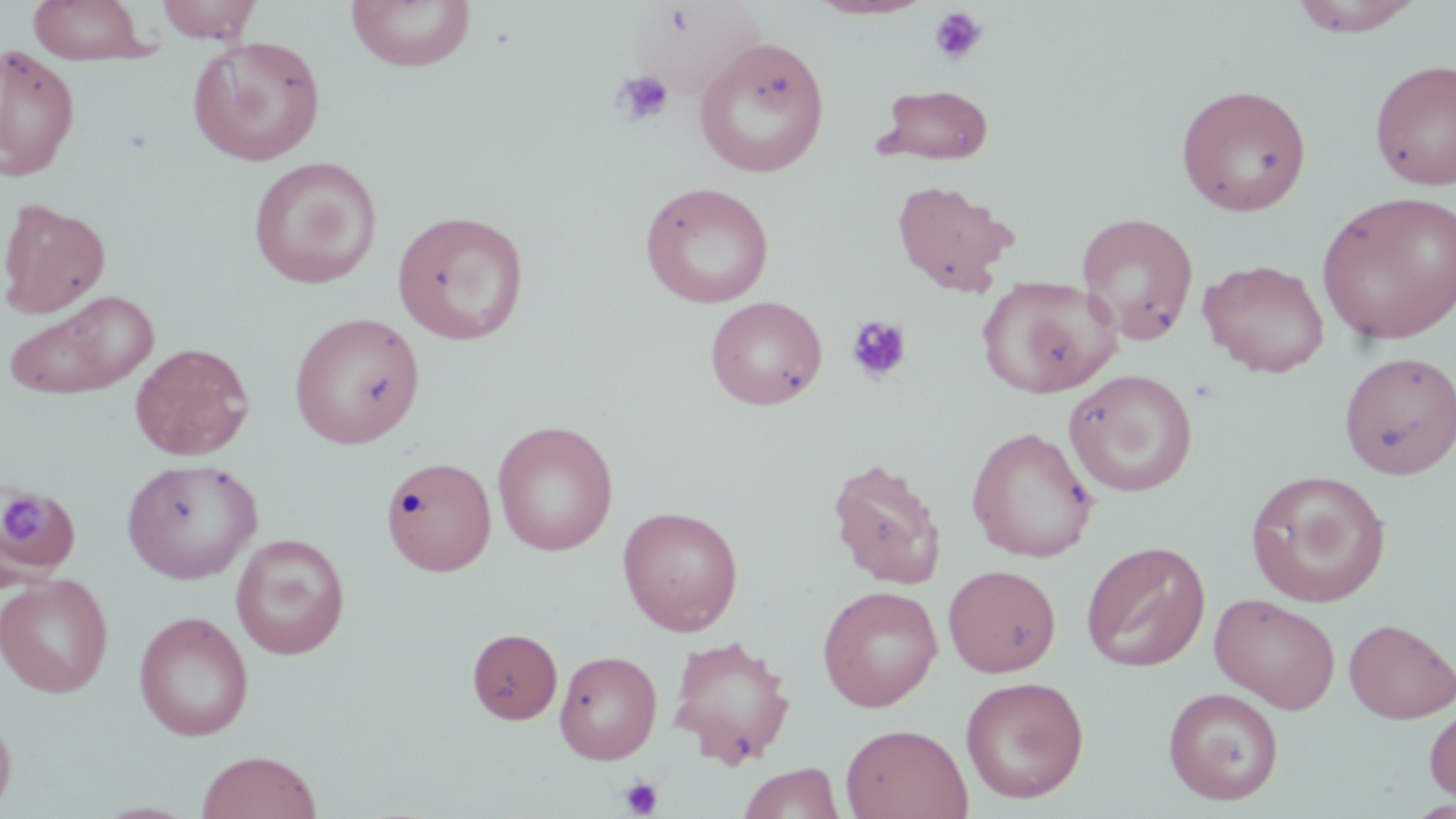

Summary:
  - Coordinate format: approximate bounding boxes as (x1, y1, x2, y2) in pixels
  - Uninfected red blood cell locations: (26, 0, 156, 65), (154, 0, 263, 43), (345, 0, 476, 73), (805, 0, 935, 20), (1289, 0, 1426, 37), (633, 4, 766, 99), (187, 35, 326, 166), (693, 37, 831, 178), (0, 44, 80, 181), (1370, 58, 1456, 190), (874, 84, 995, 165), (1176, 84, 1312, 217), (248, 156, 382, 289), (890, 179, 1019, 296), (639, 181, 776, 308), (1316, 189, 1456, 346), (0, 197, 110, 319), (391, 209, 530, 345), (1076, 211, 1200, 345), (1199, 259, 1330, 378), (976, 274, 1121, 399), (3, 290, 159, 400), (705, 295, 828, 410), (289, 311, 425, 449), (129, 342, 255, 461), (1338, 350, 1456, 478), (1063, 368, 1199, 497), (492, 420, 619, 556), (966, 426, 1099, 563), (381, 456, 496, 576), (827, 457, 947, 588), (121, 458, 263, 584), (1245, 470, 1391, 607), (0, 482, 80, 583), (617, 506, 744, 636), (230, 533, 351, 660), (1081, 540, 1211, 672), (943, 564, 1062, 677), (0, 574, 113, 698), (817, 585, 943, 711), (1210, 593, 1341, 713), (133, 611, 254, 742), (1343, 618, 1456, 723), (466, 627, 563, 724), (666, 633, 797, 768), (554, 650, 662, 763), (960, 675, 1089, 803), (1163, 686, 1285, 805), (1424, 703, 1456, 806), (0, 708, 16, 815), (840, 723, 973, 819), (196, 749, 322, 819), (737, 762, 845, 819)
  - Platelet locations: (927, 7, 988, 66), (612, 70, 674, 128), (845, 315, 913, 384), (3, 491, 46, 546), (619, 775, 663, 817)
  - Slide-level diagnosis: no evidence of blood parasites
  - Image size: 1456×819 pixels
  - Magnification: 1000x
  - Stain: May-Grünwald-Giemsa
  - Field of view: one of a larger specimen
  - Preparation: thin blood film
  - Modality: light microscopy